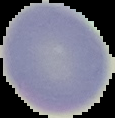
Image is 115×118 pixels. Malaria status: uninfected. Segmented cell region on a black background. From a thin blood film.